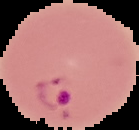
Summary:
  - Image type: segmented cell region on a black background
  - Malaria status: parasitized
  - Preparation: thin blood smear
  - Image size: 139×130 pixels